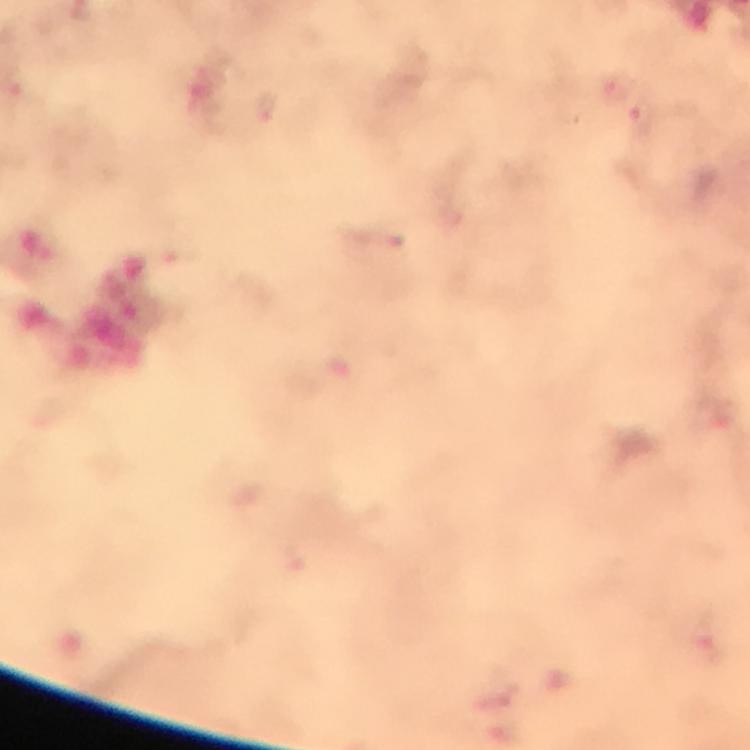
image size = 750×750 pixels
preparation = thick smear
cropped from = one field of view
stain = Giemsa
context = from a diagnostic examination for malaria
magnification = 100x
capture = smartphone photograph through a microscope
immersion oil = applied
Plasmodium parasite locations = approximate centers as {x, y} in pixels: {645, 122}